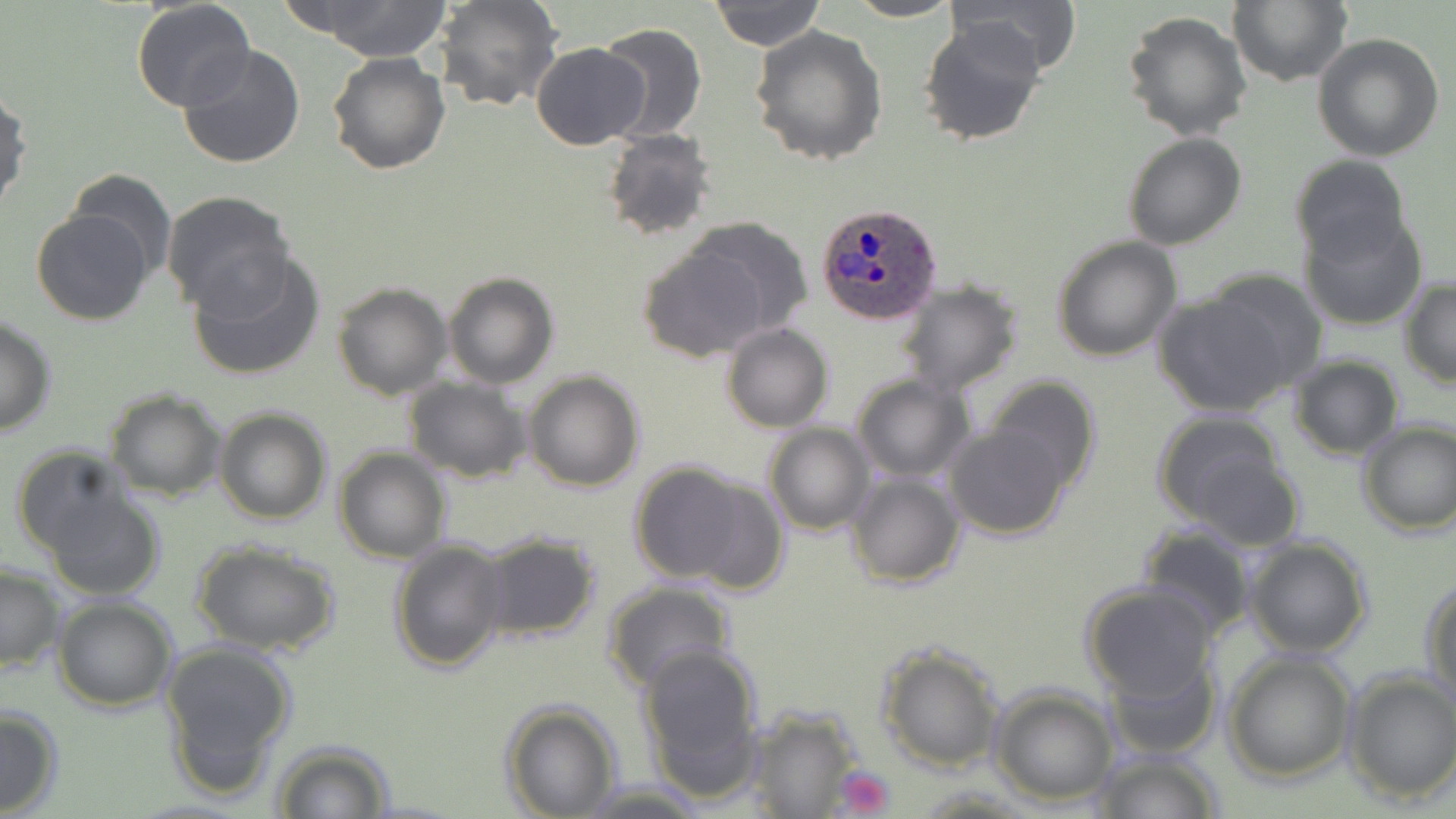 Approximate bounding boxes as [x1, y1, x2, y2] in pixels. Plasmodium ovale-infected red blood cell locations: [818, 201, 943, 326]. Platelet locations: [830, 765, 895, 818]. Uninfected red blood cell locations: [303, 0, 453, 62], [432, 0, 563, 112], [844, 0, 964, 23], [945, 0, 1082, 79], [710, 1, 826, 49], [1228, 1, 1351, 87], [131, 2, 256, 113], [1122, 10, 1253, 141], [916, 18, 1047, 148], [595, 22, 708, 143], [750, 26, 887, 165], [1312, 33, 1445, 162], [531, 42, 651, 149], [177, 45, 307, 169], [327, 51, 450, 176], [0, 85, 31, 219], [602, 127, 716, 242], [1122, 132, 1247, 250], [1288, 153, 1411, 265], [65, 170, 178, 282], [161, 190, 294, 313], [31, 207, 153, 325], [1299, 212, 1428, 332], [685, 217, 813, 337], [1051, 236, 1183, 362], [639, 244, 769, 363], [188, 250, 325, 381], [443, 271, 559, 388], [1398, 279, 1456, 387], [896, 280, 1025, 396], [331, 281, 452, 401], [1155, 281, 1313, 416], [0, 315, 57, 438], [721, 324, 834, 433], [1287, 354, 1404, 458], [523, 370, 645, 492], [851, 374, 973, 482], [403, 376, 530, 481], [984, 377, 1100, 493], [104, 389, 226, 501], [213, 406, 332, 525], [1154, 411, 1291, 528], [945, 421, 1071, 539], [1356, 421, 1456, 535], [763, 423, 877, 535], [11, 446, 135, 557], [335, 448, 451, 563], [1184, 452, 1304, 551], [628, 460, 759, 585], [845, 472, 965, 589], [678, 475, 789, 596], [43, 491, 165, 600], [1135, 524, 1258, 640], [184, 533, 330, 771], [474, 533, 602, 642], [1243, 534, 1373, 658], [389, 538, 511, 671], [192, 540, 339, 656], [0, 565, 63, 676], [1421, 576, 1455, 703], [603, 582, 735, 694], [1078, 583, 1221, 701], [52, 597, 178, 712], [158, 640, 298, 791], [637, 641, 764, 780], [876, 642, 1004, 771], [1222, 650, 1356, 783], [1107, 654, 1220, 760], [1343, 670, 1456, 804], [989, 686, 1117, 805], [500, 702, 621, 818], [0, 703, 63, 817], [739, 708, 869, 816], [271, 741, 397, 819], [1090, 749, 1223, 818], [579, 780, 707, 816]. Slide-level diagnosis: Plasmodium ovale. 1000x magnification. May-Grünwald-Giemsa stain. Thin blood smear. Single field of view. Optical microscopy. Image is 1456×819 pixels.